Report the malaria status of this cell.
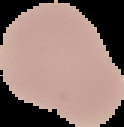

Uninfected.

{
  "image_type": "segmented cell region on a black background",
  "preparation": "thin blood smear",
  "image_size": "124×127 pixels"
}